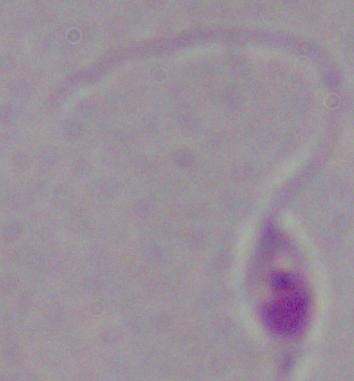 Captured at 1000x magnification. A Leishmania parasite is shown. Photomicrograph.